Identify the cell.
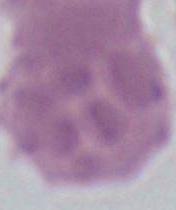
An erythrocyte.

1000x magnification. Photomicrograph.